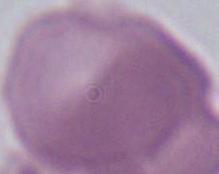

Summary:
  - Magnification: 1000x
  - Modality: micrograph
  - Identification: red blood cell